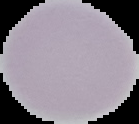 Result: negative for Plasmodium parasites. Segmented cell region on a black background. From a thin blood film. Image is 139×124 pixels.